Outline each Plasmodium malariae-infected red blood cell.
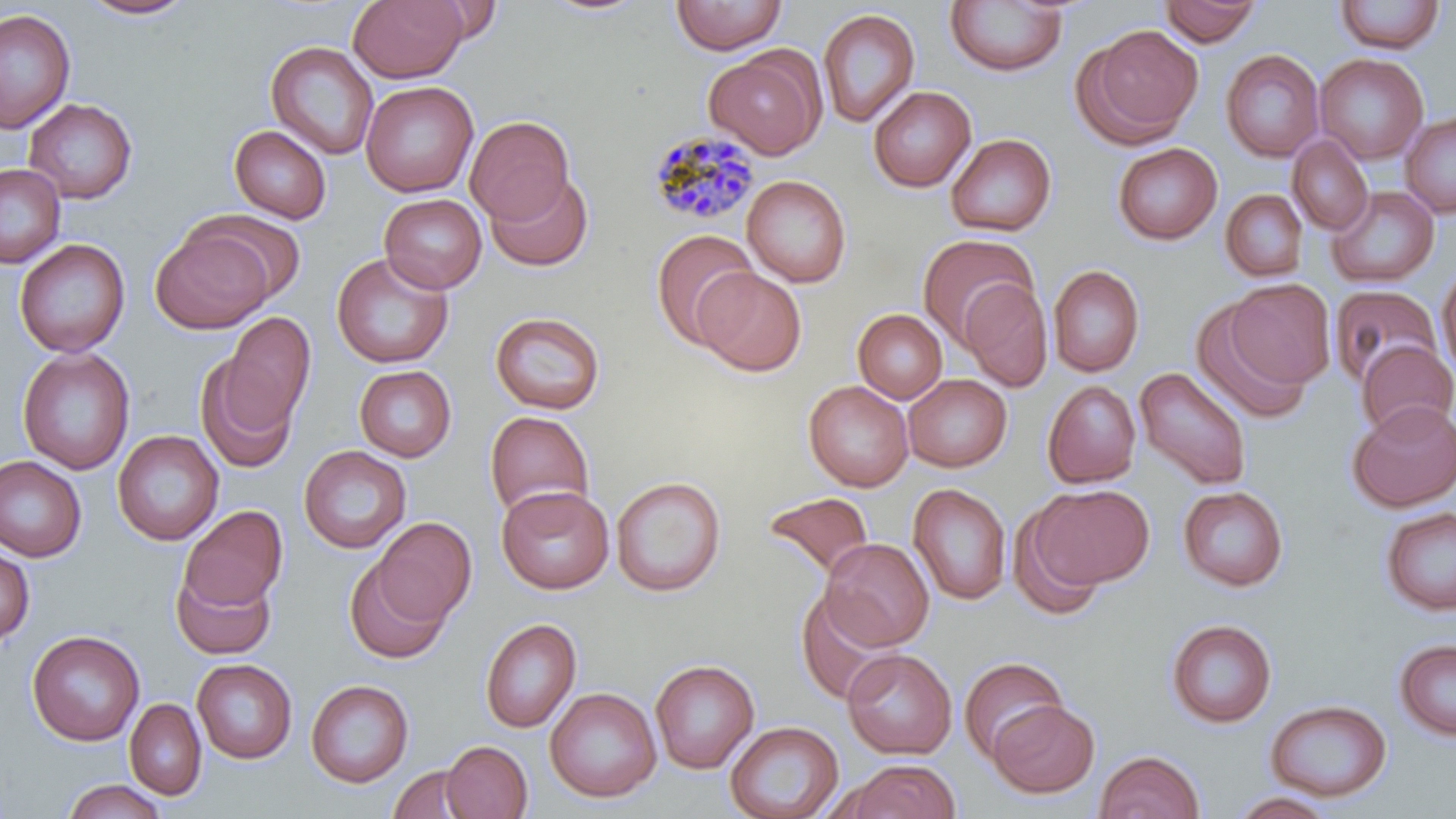

Approximate bounding boxes as named x1/y1/x2/y2 corners in pixels.
Plasmodium malariae-infected red blood cells: (x1=645, y1=129, x2=763, y2=227).

slide-level diagnosis = Plasmodium malariae
stain = May-Grünwald-Giemsa
preparation = thin blood smear
field of view = single
magnification = 1000x
image size = 1456×819 pixels
uninfected red blood cell locations = approximate bounding boxes as named x1/y1/x2/y2 corners in pixels: (x1=536, y1=0, x2=656, y2=18), (x1=670, y1=0, x2=788, y2=54), (x1=76, y1=1, x2=198, y2=21), (x1=347, y1=1, x2=468, y2=83), (x1=405, y1=1, x2=507, y2=46), (x1=945, y1=1, x2=1068, y2=77), (x1=1159, y1=1, x2=1264, y2=46), (x1=1332, y1=1, x2=1447, y2=55), (x1=0, y1=8, x2=76, y2=134), (x1=817, y1=8, x2=920, y2=128), (x1=1077, y1=24, x2=1204, y2=146), (x1=266, y1=41, x2=379, y2=160), (x1=704, y1=48, x2=826, y2=159), (x1=1221, y1=49, x2=1324, y2=162), (x1=1314, y1=53, x2=1429, y2=164), (x1=361, y1=80, x2=479, y2=197), (x1=868, y1=86, x2=976, y2=192), (x1=24, y1=98, x2=138, y2=204), (x1=1400, y1=110, x2=1456, y2=217), (x1=465, y1=115, x2=574, y2=224), (x1=229, y1=125, x2=332, y2=223), (x1=945, y1=133, x2=1057, y2=237), (x1=1288, y1=135, x2=1374, y2=235), (x1=1112, y1=142, x2=1222, y2=245), (x1=0, y1=163, x2=66, y2=268), (x1=484, y1=170, x2=593, y2=272), (x1=742, y1=175, x2=852, y2=288), (x1=1327, y1=186, x2=1440, y2=287), (x1=1220, y1=189, x2=1308, y2=281), (x1=379, y1=193, x2=487, y2=294), (x1=186, y1=210, x2=308, y2=305), (x1=151, y1=225, x2=274, y2=334), (x1=650, y1=229, x2=760, y2=349), (x1=916, y1=233, x2=1038, y2=346), (x1=14, y1=238, x2=130, y2=358), (x1=331, y1=251, x2=455, y2=369), (x1=1048, y1=264, x2=1145, y2=377), (x1=1436, y1=265, x2=1455, y2=382), (x1=694, y1=268, x2=807, y2=376), (x1=960, y1=277, x2=1053, y2=392), (x1=1226, y1=278, x2=1335, y2=390), (x1=1330, y1=284, x2=1443, y2=390), (x1=1190, y1=298, x2=1312, y2=425), (x1=853, y1=309, x2=948, y2=403), (x1=490, y1=311, x2=606, y2=414), (x1=222, y1=312, x2=315, y2=432), (x1=1357, y1=341, x2=1456, y2=439), (x1=17, y1=347, x2=136, y2=475), (x1=195, y1=355, x2=299, y2=474), (x1=354, y1=364, x2=457, y2=462), (x1=1134, y1=367, x2=1252, y2=490), (x1=903, y1=374, x2=1011, y2=472), (x1=804, y1=380, x2=914, y2=492), (x1=1042, y1=380, x2=1142, y2=488), (x1=1346, y1=400, x2=1456, y2=512), (x1=484, y1=410, x2=596, y2=520), (x1=112, y1=429, x2=224, y2=546), (x1=299, y1=445, x2=412, y2=553), (x1=0, y1=456, x2=86, y2=561), (x1=611, y1=476, x2=726, y2=596), (x1=908, y1=483, x2=1012, y2=605), (x1=1032, y1=484, x2=1154, y2=588), (x1=496, y1=485, x2=615, y2=594), (x1=1178, y1=486, x2=1289, y2=591), (x1=762, y1=492, x2=875, y2=581), (x1=1009, y1=504, x2=1109, y2=621), (x1=178, y1=505, x2=288, y2=613), (x1=1380, y1=506, x2=1456, y2=617), (x1=372, y1=516, x2=476, y2=627), (x1=820, y1=538, x2=934, y2=651), (x1=0, y1=547, x2=35, y2=647), (x1=344, y1=556, x2=452, y2=664), (x1=170, y1=562, x2=278, y2=660), (x1=795, y1=588, x2=901, y2=705), (x1=479, y1=618, x2=582, y2=734), (x1=1165, y1=618, x2=1277, y2=728), (x1=27, y1=630, x2=145, y2=746), (x1=1394, y1=638, x2=1456, y2=742), (x1=842, y1=649, x2=957, y2=759), (x1=959, y1=656, x2=1068, y2=763), (x1=192, y1=659, x2=297, y2=764), (x1=650, y1=659, x2=760, y2=774), (x1=306, y1=679, x2=414, y2=787), (x1=544, y1=687, x2=662, y2=803), (x1=124, y1=698, x2=207, y2=800), (x1=1265, y1=699, x2=1392, y2=802), (x1=988, y1=700, x2=1100, y2=798), (x1=724, y1=720, x2=844, y2=819), (x1=441, y1=740, x2=533, y2=819), (x1=1094, y1=749, x2=1205, y2=819), (x1=845, y1=759, x2=961, y2=819), (x1=388, y1=764, x2=479, y2=819), (x1=60, y1=778, x2=167, y2=819), (x1=1229, y1=791, x2=1339, y2=818)
modality = light microscopy